Report the malaria status of this cell.
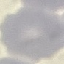
Uninfected.

Summary:
  - Image type: automatically extracted cell patch, resized to 64 × 64 pixels
  - Capture: smartphone camera at the microscope eyepiece
  - Stain: Giemsa
  - Preparation: thin blood film